Assess this cell for malaria.
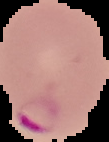
It is parasitized.

image type = segmented cell region on a black background
image size = 109×142 pixels
preparation = thin blood smear